Name the blood parasite species.
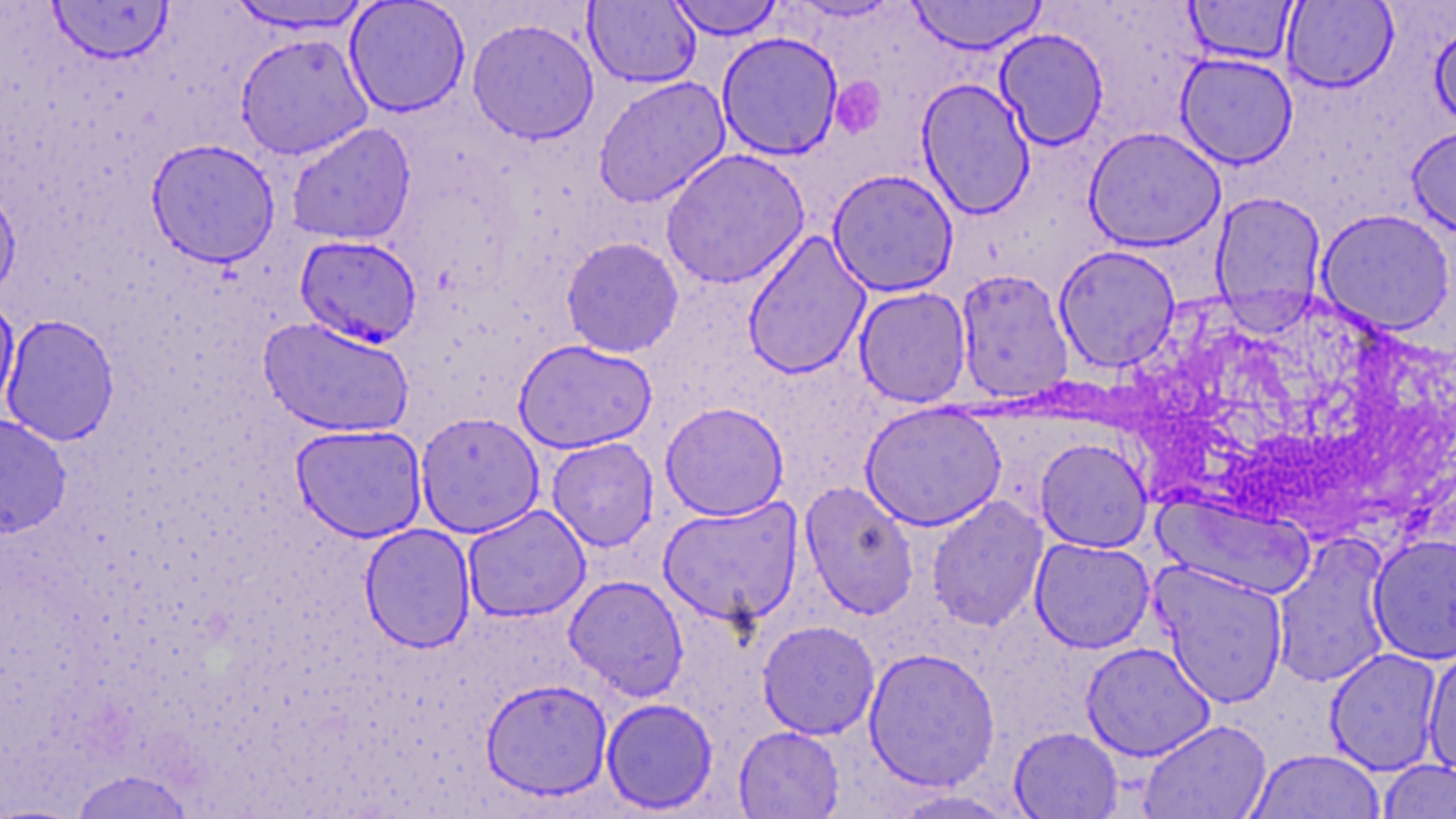
Plasmodium falciparum.

stain = May-Grünwald-Giemsa
uninfected red blood cell locations = approximate bounding boxes as named x1/y1/x2/y2 corners in pixels: (x1=344, y1=0, x2=471, y2=117), (x1=665, y1=0, x2=785, y2=40), (x1=907, y1=0, x2=1047, y2=54), (x1=1184, y1=0, x2=1299, y2=65), (x1=47, y1=1, x2=174, y2=64), (x1=226, y1=1, x2=377, y2=35), (x1=583, y1=1, x2=701, y2=88), (x1=1282, y1=1, x2=1399, y2=93), (x1=344, y1=10, x2=600, y2=125), (x1=466, y1=17, x2=600, y2=144), (x1=1430, y1=17, x2=1456, y2=132), (x1=994, y1=28, x2=1109, y2=150), (x1=716, y1=31, x2=844, y2=161), (x1=235, y1=33, x2=373, y2=160), (x1=1175, y1=53, x2=1298, y2=169), (x1=593, y1=76, x2=731, y2=207), (x1=916, y1=78, x2=1036, y2=219), (x1=286, y1=123, x2=417, y2=246), (x1=1407, y1=124, x2=1456, y2=238), (x1=1083, y1=126, x2=1226, y2=251), (x1=145, y1=138, x2=281, y2=267), (x1=660, y1=148, x2=810, y2=289), (x1=827, y1=168, x2=959, y2=297), (x1=0, y1=186, x2=21, y2=303), (x1=1210, y1=192, x2=1327, y2=326), (x1=1316, y1=209, x2=1455, y2=335), (x1=742, y1=231, x2=871, y2=380), (x1=561, y1=236, x2=684, y2=358), (x1=1053, y1=244, x2=1181, y2=373), (x1=955, y1=269, x2=1074, y2=403), (x1=853, y1=286, x2=972, y2=407), (x1=0, y1=295, x2=20, y2=417), (x1=1, y1=314, x2=120, y2=446), (x1=258, y1=316, x2=414, y2=438), (x1=513, y1=339, x2=658, y2=454), (x1=660, y1=401, x2=789, y2=521), (x1=860, y1=401, x2=1007, y2=531), (x1=415, y1=411, x2=545, y2=538), (x1=0, y1=413, x2=71, y2=538), (x1=290, y1=423, x2=428, y2=542), (x1=546, y1=437, x2=659, y2=551), (x1=1035, y1=438, x2=1153, y2=553), (x1=800, y1=481, x2=919, y2=619), (x1=1155, y1=494, x2=1316, y2=600), (x1=926, y1=495, x2=1048, y2=631), (x1=658, y1=498, x2=803, y2=628), (x1=462, y1=505, x2=591, y2=623), (x1=359, y1=523, x2=476, y2=653), (x1=1368, y1=533, x2=1456, y2=664), (x1=1272, y1=534, x2=1393, y2=688), (x1=1030, y1=537, x2=1155, y2=653), (x1=1151, y1=562, x2=1289, y2=707), (x1=563, y1=575, x2=689, y2=700), (x1=757, y1=620, x2=880, y2=740), (x1=1080, y1=641, x2=1216, y2=762), (x1=1422, y1=645, x2=1456, y2=780), (x1=863, y1=647, x2=1000, y2=791), (x1=1324, y1=648, x2=1445, y2=775), (x1=481, y1=678, x2=613, y2=801), (x1=600, y1=697, x2=719, y2=814), (x1=1139, y1=719, x2=1272, y2=819), (x1=733, y1=725, x2=845, y2=818), (x1=1008, y1=727, x2=1124, y2=818), (x1=1246, y1=749, x2=1386, y2=819), (x1=1377, y1=760, x2=1456, y2=818), (x1=68, y1=769, x2=195, y2=818), (x1=886, y1=788, x2=1019, y2=818)
field of view = single
preparation = thin blood smear
Plasmodium falciparum-infected red blood cell locations = approximate bounding boxes as named x1/y1/x2/y2 corners in pixels: (x1=294, y1=235, x2=423, y2=348)
modality = optical microscopy
platelet locations = approximate bounding boxes as named x1/y1/x2/y2 corners in pixels: (x1=831, y1=77, x2=884, y2=139)
magnification = 1000x
image size = 1456×819 pixels